Name the blood parasite species.
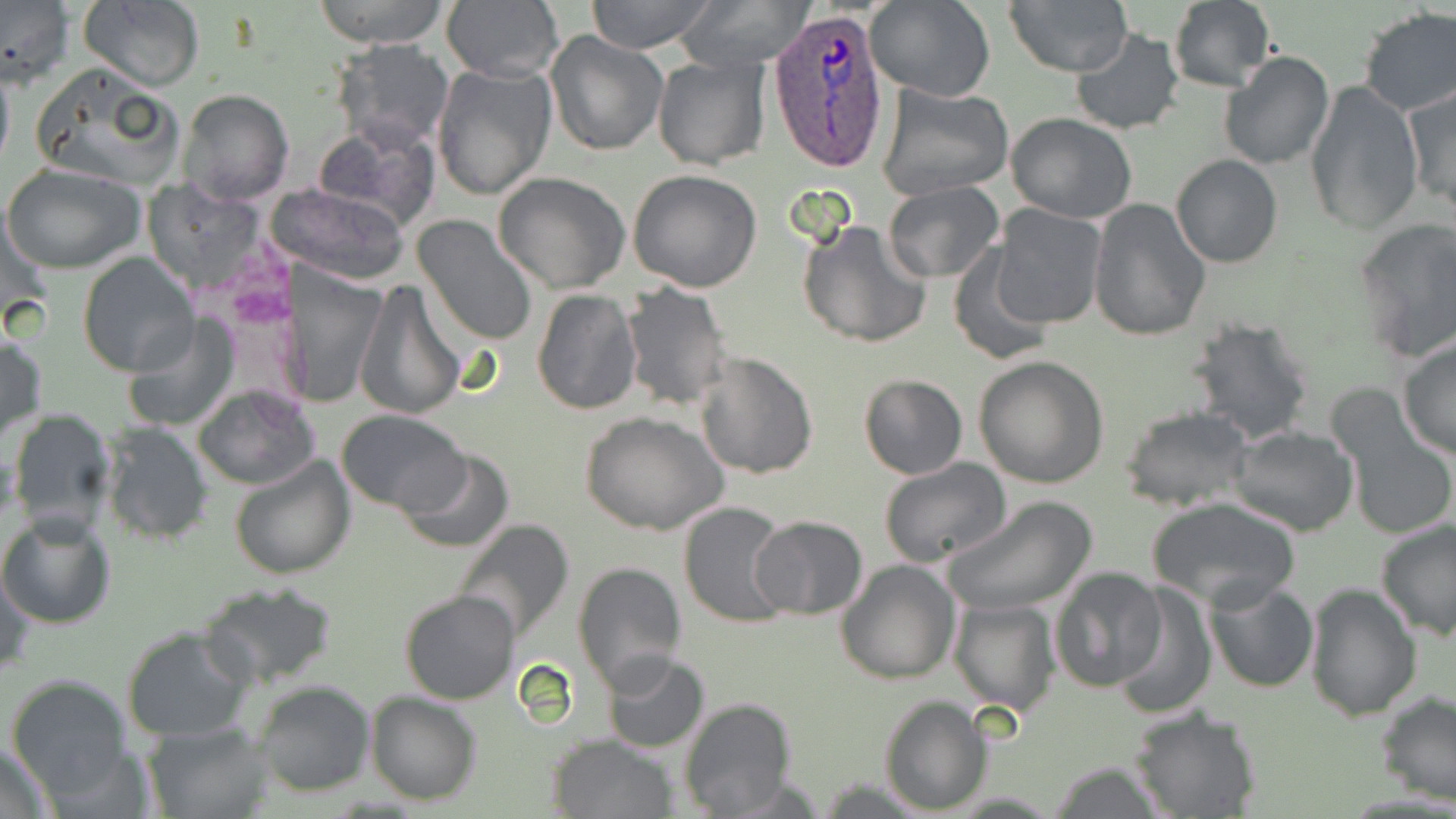
Plasmodium ovale.

Summary:
  - Coordinate format: approximate bounding boxes as [x1, y1, x2, y2] in pixels
  - Plasmodium ovale-infected red blood cell locations: [764, 8, 891, 171]
  - Uninfected red blood cell locations: [0, 0, 74, 85], [76, 0, 206, 91], [313, 0, 450, 48], [440, 0, 563, 83], [584, 0, 717, 54], [677, 0, 813, 72], [866, 0, 996, 103], [1005, 0, 1132, 76], [1167, 1, 1276, 92], [1358, 7, 1455, 117], [1069, 28, 1186, 135], [546, 31, 666, 156], [331, 39, 453, 150], [1219, 51, 1334, 171], [652, 55, 772, 170], [0, 58, 14, 176], [30, 62, 186, 189], [432, 62, 558, 200], [1306, 81, 1423, 236], [874, 82, 1013, 203], [1403, 83, 1455, 216], [177, 90, 294, 206], [1007, 113, 1137, 222], [312, 119, 439, 230], [1170, 155, 1283, 269], [1, 162, 146, 274], [628, 168, 764, 294], [492, 171, 631, 295], [881, 181, 1006, 282], [275, 182, 412, 287], [1089, 199, 1212, 341], [991, 205, 1107, 328], [413, 217, 538, 348], [796, 219, 933, 352], [1353, 220, 1456, 363], [946, 243, 1057, 366], [78, 253, 199, 375], [283, 267, 386, 408], [352, 279, 465, 420], [620, 283, 732, 412], [532, 288, 642, 413], [124, 311, 239, 433], [1184, 317, 1316, 446], [0, 328, 46, 443], [1397, 340, 1456, 460], [693, 352, 819, 479], [975, 356, 1110, 489], [859, 373, 968, 479], [193, 384, 318, 489], [1119, 406, 1253, 512], [335, 408, 471, 513], [6, 409, 119, 535], [1339, 410, 1456, 542], [581, 412, 730, 536], [96, 420, 215, 546], [1227, 424, 1360, 536], [394, 447, 515, 553], [229, 453, 354, 580], [877, 457, 1011, 570], [944, 497, 1098, 617], [1145, 497, 1303, 610], [677, 501, 793, 629], [0, 510, 117, 630], [751, 514, 868, 620], [449, 518, 577, 645], [1373, 519, 1456, 640], [571, 558, 688, 691], [836, 559, 961, 684], [1, 564, 34, 682], [1051, 566, 1168, 692], [1204, 578, 1319, 693], [197, 582, 339, 692], [1303, 582, 1422, 722], [1111, 583, 1217, 719], [398, 588, 520, 705], [950, 598, 1061, 714], [122, 626, 253, 743], [601, 652, 710, 753], [7, 674, 133, 804], [250, 679, 375, 797], [1376, 691, 1456, 805], [365, 692, 483, 805], [879, 693, 991, 812], [678, 697, 795, 818], [1126, 706, 1262, 818], [144, 720, 273, 818], [547, 734, 675, 818], [1, 737, 56, 818], [1047, 762, 1168, 818]
  - Magnification: 1000x
  - Preparation: thin blood film
  - Field of view: single
  - Stain: May-Grünwald-Giemsa
  - Modality: optical microscopy
  - Image size: 1456×819 pixels